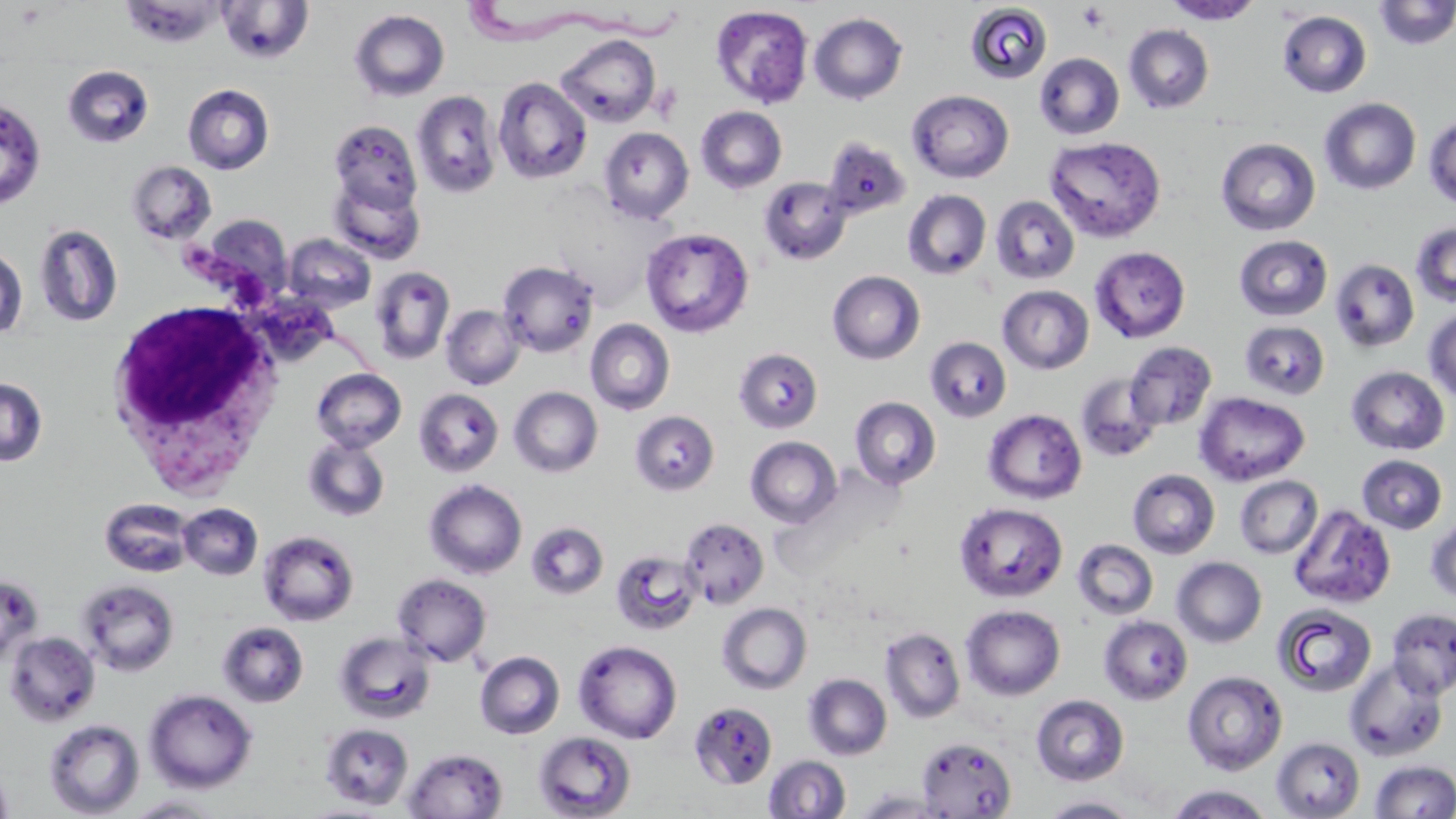
slide_level_diagnosis: Trypanosoma brucei
magnification: 1000x
white_blood_cell_locations: 'approximate bounding boxes as [x1, y1, x2, y2] in pixels: [104, 295, 286, 494]'
trypanosoma_brucei_locations: 'approximate bounding boxes as [x1, y1, x2, y2] in pixels: [460, 0, 686, 53], [174, 242, 387, 376]'
platelet_locations: 'approximate bounding boxes as [x1, y1, x2, y2] in pixels: [15, 3, 46, 28], [1076, 3, 1111, 33]'
uninfected_red_blood_cell_locations: 'approximate bounding boxes as [x1, y1, x2, y2] in pixels: [121, 1, 226, 48], [216, 1, 314, 64], [1163, 1, 1264, 25], [1373, 1, 1456, 50], [965, 2, 1053, 85], [711, 5, 814, 108], [349, 9, 450, 102], [1277, 10, 1372, 98], [809, 12, 908, 105], [1124, 24, 1214, 113], [554, 33, 661, 127], [1034, 52, 1125, 140], [62, 65, 154, 148], [493, 77, 592, 184], [183, 83, 274, 175], [907, 89, 1014, 183], [412, 90, 501, 199], [1319, 97, 1421, 195], [0, 98, 46, 209], [695, 106, 787, 194], [1423, 114, 1456, 209], [329, 119, 422, 215], [599, 127, 693, 224], [1044, 135, 1167, 243], [821, 136, 911, 221], [1215, 137, 1321, 236], [126, 160, 217, 245], [328, 175, 425, 264], [759, 176, 851, 265], [902, 189, 991, 280], [990, 195, 1080, 285], [196, 214, 294, 305], [1410, 221, 1456, 307], [34, 223, 123, 328], [641, 227, 754, 338], [283, 233, 376, 313], [1234, 234, 1333, 321], [1090, 246, 1191, 343], [0, 247, 28, 340], [1330, 258, 1420, 353], [497, 260, 600, 358], [370, 265, 455, 364], [827, 270, 925, 364], [997, 285, 1094, 374], [441, 305, 524, 390], [1423, 307, 1456, 404], [585, 319, 675, 415], [1239, 321, 1330, 400], [925, 336, 1012, 422], [1124, 341, 1217, 431], [734, 348, 823, 434], [1346, 366, 1450, 456], [312, 368, 406, 452], [1075, 373, 1162, 463], [0, 377, 48, 467], [509, 386, 602, 477], [413, 388, 504, 477], [1194, 392, 1310, 486], [849, 396, 941, 489], [984, 409, 1087, 504], [630, 410, 720, 495], [302, 436, 391, 522], [745, 436, 842, 528], [1357, 455, 1447, 534], [1128, 468, 1220, 558], [1235, 475, 1323, 559], [424, 479, 527, 579], [99, 498, 195, 578], [954, 502, 1067, 601], [178, 503, 263, 581], [1289, 504, 1395, 609], [1425, 516, 1456, 604], [680, 517, 769, 608], [526, 522, 609, 600], [259, 530, 359, 626], [1072, 539, 1158, 620], [611, 548, 702, 636], [1172, 556, 1267, 647], [392, 573, 492, 667], [0, 574, 43, 667], [76, 579, 179, 676], [717, 602, 812, 694], [1273, 603, 1377, 697], [960, 605, 1065, 700], [1386, 607, 1456, 699], [1099, 615, 1193, 704], [218, 621, 308, 707], [879, 627, 966, 723], [4, 631, 100, 727], [335, 632, 435, 723], [573, 640, 682, 744], [475, 651, 565, 739], [1344, 659, 1449, 762], [1182, 670, 1287, 775], [804, 673, 892, 760], [144, 689, 257, 793], [1031, 694, 1129, 785], [689, 701, 777, 789], [43, 719, 144, 818], [320, 723, 414, 810], [533, 731, 637, 819], [917, 736, 1017, 817], [1271, 737, 1365, 819], [403, 748, 508, 819], [763, 755, 851, 818], [1370, 760, 1456, 818], [0, 763, 14, 819], [1164, 785, 1275, 818], [852, 789, 952, 818], [124, 795, 227, 817], [1040, 796, 1141, 818]'
preparation: thin blood film
field_of_view: single
modality: optical microscopy
image_size: 1456×819 pixels
stain: May-Grünwald-Giemsa